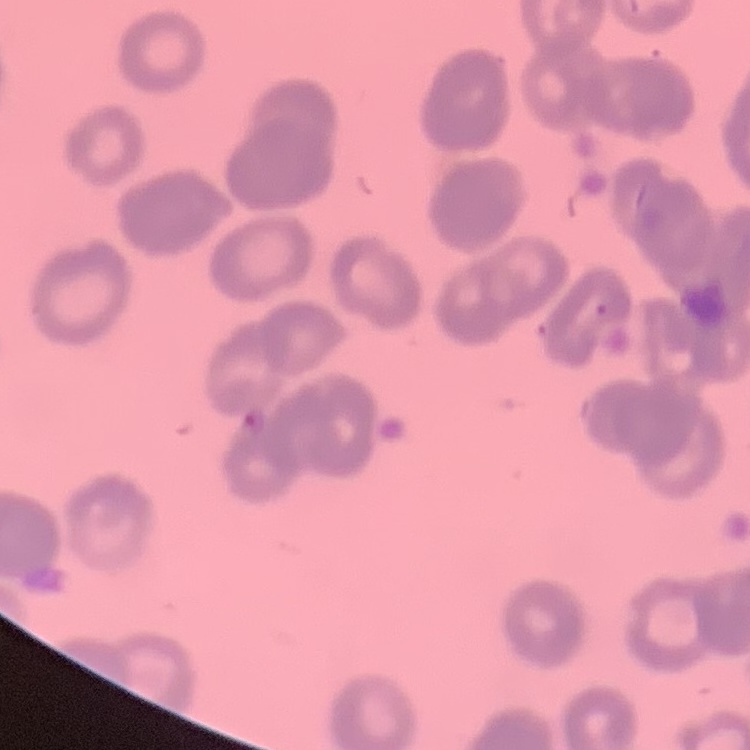 The red blood cells show rouleaux formation. Thin peripheral smear. Field's or Giemsa stain. Square crop of a larger photomicrograph.